Give the extent of all uninfected red blood cells.
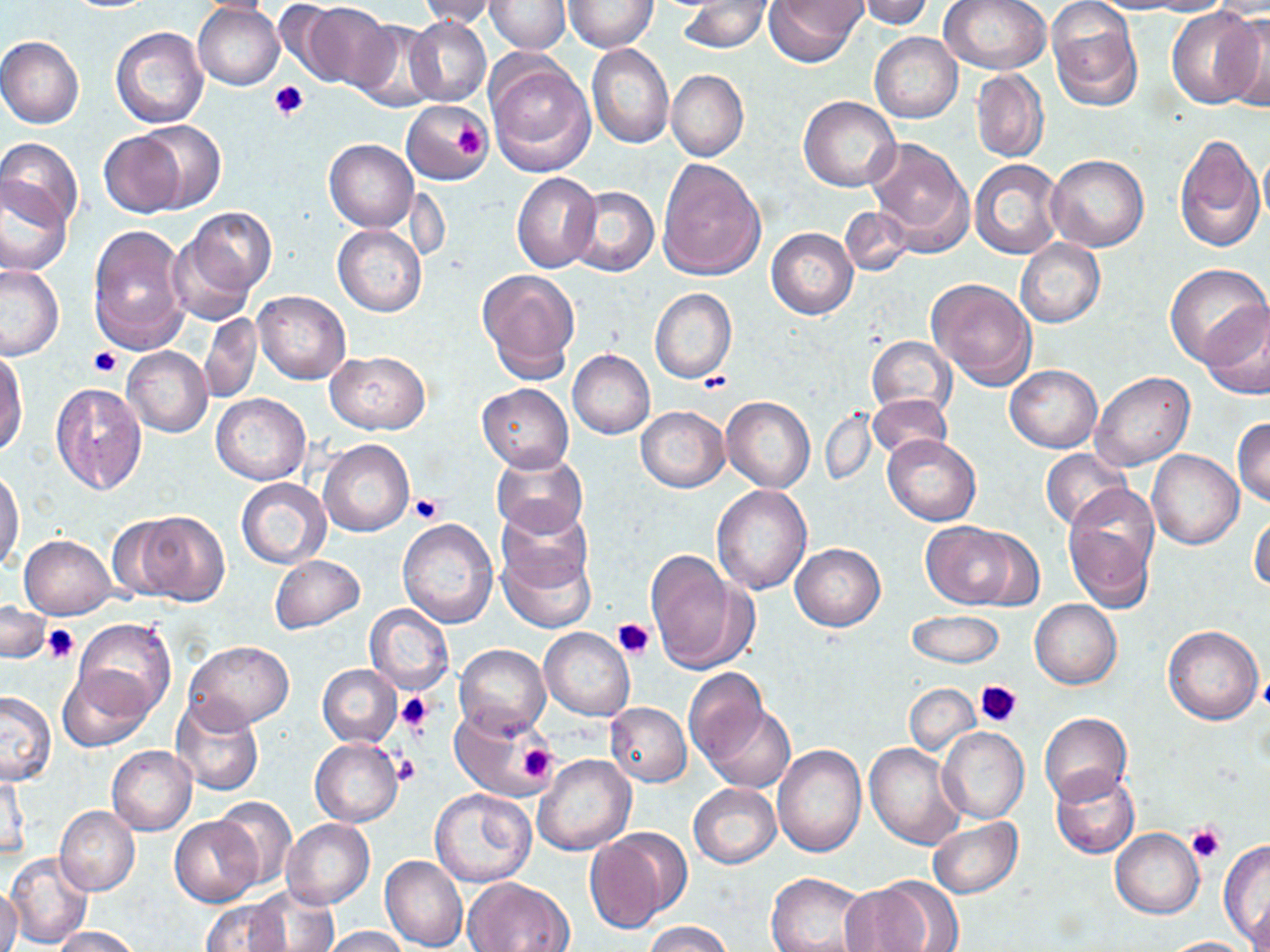
Approximate bounding boxes as (x1,y1)-(x2,y2) corner pairs in pixels.
Uninfected red blood cells: (61,0)-(156,12), (187,0)-(283,15), (414,0)-(506,27), (763,0)-(866,68), (938,0)-(1049,75), (1046,0)-(1143,112), (1087,0)-(1191,14), (1137,0)-(1231,16), (485,1)-(571,53), (563,1)-(657,52), (854,1)-(936,28), (680,2)-(771,54), (1210,2)-(1270,20), (294,3)-(392,91), (193,5)-(285,90), (1166,7)-(1259,109), (1220,12)-(1270,113), (406,15)-(491,107), (347,18)-(441,113), (110,25)-(209,128), (870,31)-(963,123), (0,36)-(83,129), (587,44)-(673,150), (487,57)-(596,175), (970,69)-(1049,163), (666,70)-(748,161), (799,96)-(901,192), (400,101)-(491,183), (134,120)-(226,210), (100,129)-(192,218), (1174,132)-(1264,252), (867,138)-(973,252), (1,139)-(84,234), (324,139)-(418,232), (1258,142)-(1270,232), (1046,154)-(1149,252), (657,159)-(766,282), (970,159)-(1062,259), (512,171)-(601,272), (0,175)-(72,277), (565,185)-(658,277), (839,206)-(914,277), (179,207)-(277,297), (88,224)-(189,355), (333,224)-(426,316), (166,227)-(259,327), (767,227)-(858,319), (1015,240)-(1105,327), (0,262)-(64,359), (1163,262)-(1269,370), (477,268)-(581,383), (927,279)-(1038,389), (650,289)-(737,384), (252,291)-(351,384), (1202,301)-(1270,400), (199,314)-(263,403), (867,336)-(955,417), (122,346)-(212,436), (325,350)-(430,434), (568,350)-(654,439), (0,351)-(28,456), (1005,364)-(1102,452), (1089,371)-(1194,473), (50,381)-(148,497), (478,384)-(573,471), (211,393)-(310,484), (867,394)-(951,461), (721,395)-(815,493), (636,406)-(729,492), (821,410)-(876,485), (1233,417)-(1270,508), (882,434)-(980,526), (319,439)-(414,537), (1041,448)-(1132,530), (1148,450)-(1243,549), (491,451)-(587,536), (1,467)-(24,575), (237,477)-(330,568), (713,484)-(812,595), (1063,489)-(1160,612), (494,503)-(594,599), (120,510)-(228,606), (1249,512)-(1270,593), (398,519)-(498,629), (921,522)-(1027,609), (19,534)-(115,619), (497,539)-(597,632), (790,543)-(885,631), (645,552)-(756,675), (269,555)-(365,633), (1030,599)-(1121,690), (0,601)-(50,664), (365,604)-(453,694), (908,610)-(1004,668), (73,619)-(175,717), (1162,623)-(1265,725), (539,627)-(634,721), (183,640)-(293,732), (455,644)-(550,737), (318,663)-(400,747), (57,665)-(155,753), (684,668)-(770,765), (905,683)-(979,755), (0,690)-(57,786), (172,698)-(264,796), (605,702)-(691,786), (703,705)-(795,792), (448,707)-(555,802), (1039,712)-(1131,805), (937,726)-(1029,824), (310,739)-(401,826), (864,743)-(967,851), (772,744)-(866,858), (107,745)-(197,835), (531,755)-(635,856), (68,762)-(187,884), (1050,768)-(1139,858), (1,774)-(31,863), (689,784)-(780,868), (430,787)-(536,886), (211,796)-(296,891), (55,806)-(139,896), (170,816)-(261,907), (281,818)-(374,909), (927,818)-(1023,898), (586,829)-(690,931), (1110,829)-(1204,918), (1218,840)-(1270,945), (6,851)-(94,950), (381,855)-(468,952), (766,871)-(872,952), (5,875)-(38,952), (463,877)-(573,952), (842,878)-(947,952), (1,887)-(22,952), (246,887)-(340,952), (199,898)-(290,952), (1247,898)-(1270,952), (643,921)-(734,952), (53,926)-(142,952), (321,926)-(410,952), (1159,936)-(1258,952).

Summary:
  - Platelet locations: (269,80)-(309,120), (448,115)-(489,166), (90,347)-(122,377), (698,371)-(732,394), (410,493)-(444,525), (612,617)-(656,660), (42,625)-(78,663), (976,679)-(1023,730), (397,691)-(433,735), (515,740)-(559,785), (396,754)-(421,786), (1186,824)-(1225,863)
  - Slide-level diagnosis: negative for blood parasites
  - Modality: optical microscopy
  - Magnification: 1000x
  - Preparation: thin blood smear
  - Image size: 1270×952 pixels
  - Stain: May-Grünwald-Giemsa
  - Field of view: one of a larger specimen